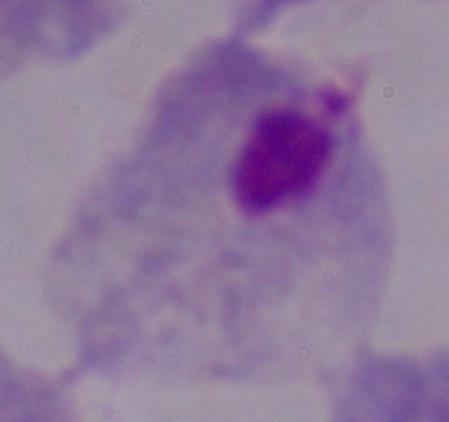

Micrograph. A trichomonad is shown. 1000x magnification.